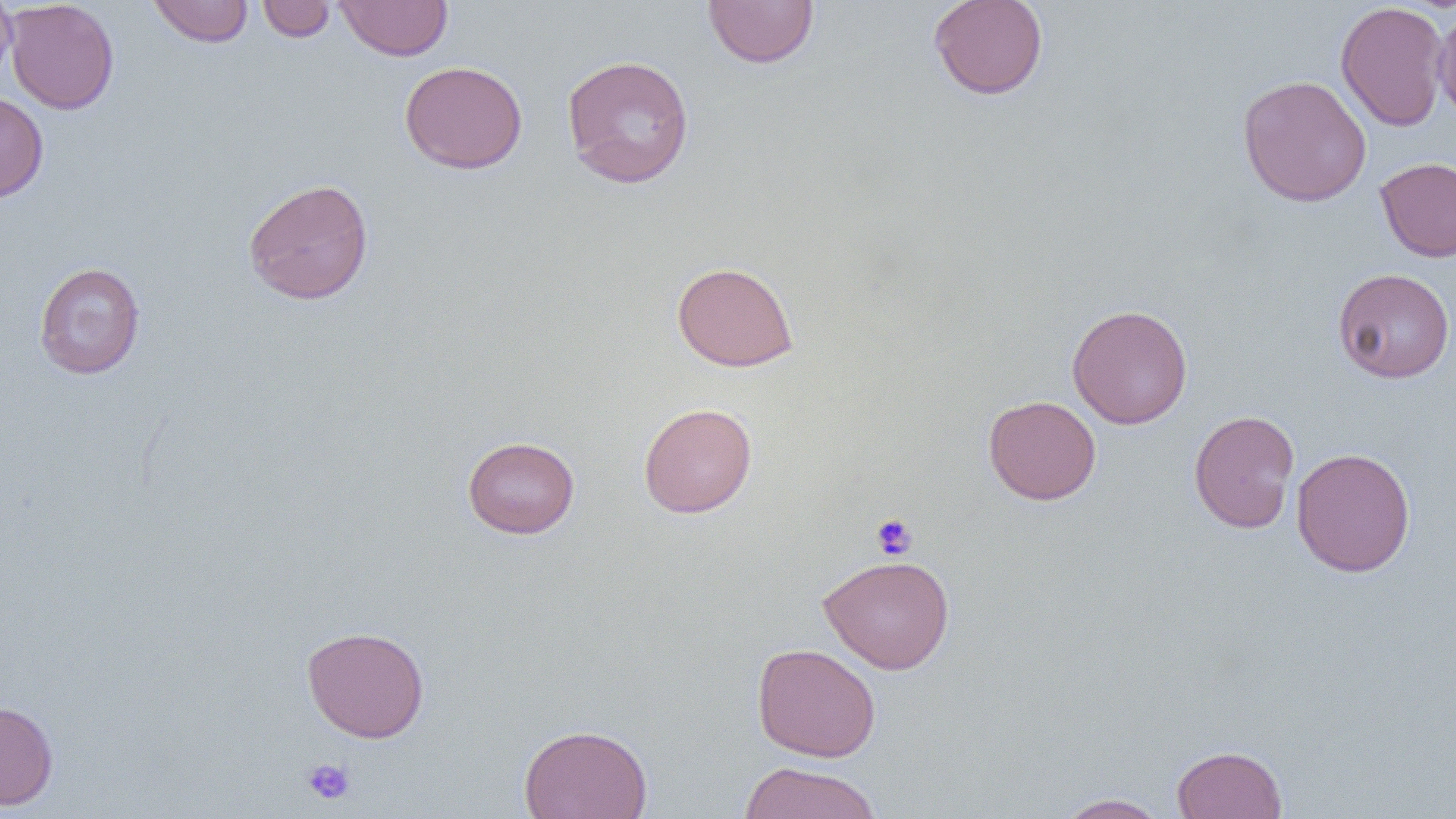
slide_level_diagnosis: negative for blood parasites
field_of_view: one of a larger specimen
magnification: 1000x
platelet_locations: 'approximate bounding boxes as (x1, y1, x2, y2) in pixels: (871, 514, 917, 560), (301, 758, 355, 805)'
preparation: thin blood smear
image_size: 1456×819 pixels
uninfected_red_blood_cell_locations: 'approximate bounding boxes as (x1, y1, x2, y2) in pixels: (0, 0, 18, 87), (5, 0, 119, 115), (257, 0, 336, 42), (703, 0, 819, 68), (927, 0, 1049, 100), (148, 1, 253, 47), (335, 1, 453, 60), (1335, 1, 1450, 132), (1432, 6, 1455, 124), (561, 53, 695, 188), (399, 60, 528, 174), (1237, 75, 1372, 207), (0, 92, 49, 203), (1375, 157, 1456, 262), (242, 178, 374, 305), (672, 261, 799, 371), (33, 262, 146, 379), (1332, 268, 1455, 383), (1067, 303, 1193, 430), (983, 395, 1101, 505), (639, 402, 757, 518), (1188, 409, 1300, 534), (462, 436, 580, 538), (1291, 447, 1416, 577), (818, 554, 955, 674), (302, 625, 430, 743), (752, 642, 881, 762), (0, 700, 59, 810), (518, 723, 653, 819), (1171, 745, 1287, 818), (738, 760, 884, 819), (1056, 792, 1170, 819)'
modality: light microscopy